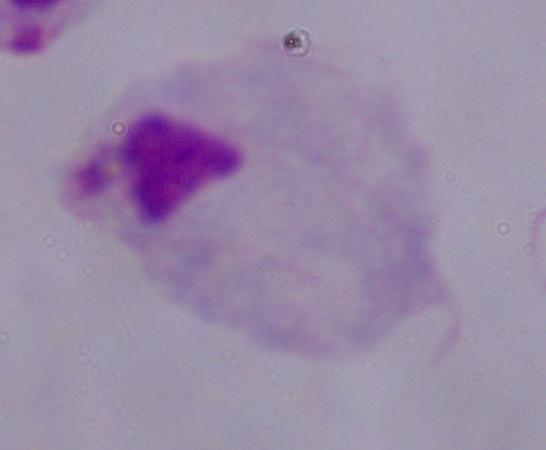

{
  "modality": "micrograph",
  "identification": "trichomonad",
  "magnification": "1000x"
}